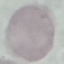

Result: negative for malaria parasites. Acquired by smartphone through the microscope eyepiece. Cell patch, automatically extracted from a larger field of view and resized to 64 × 64 pixels. Giemsa-stained preparation. Thin blood smear.